Give the position of every malaria parasite.
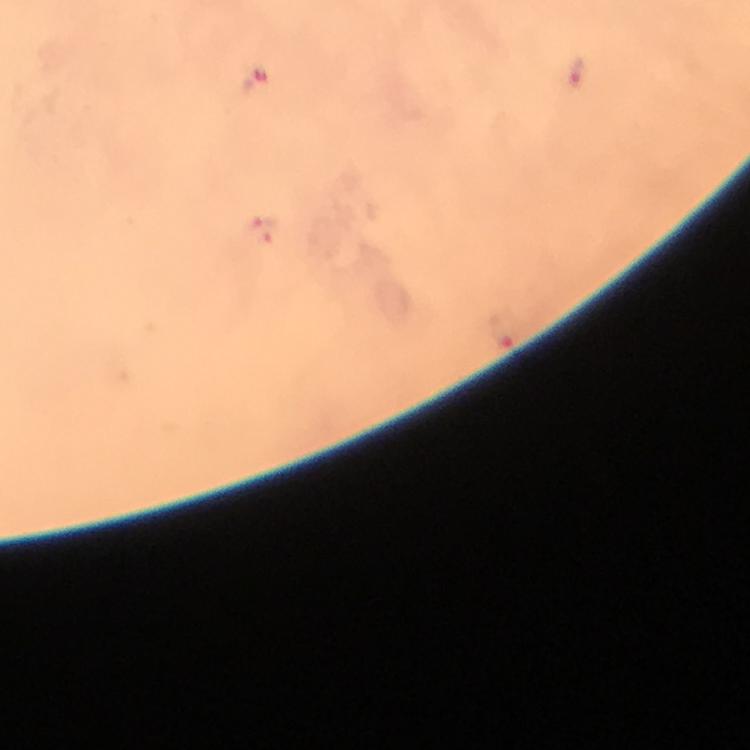
Approximate centers as {x, y} in pixels.
Malaria parasites: {576, 73}, {255, 80}, {260, 229}, {502, 331}.

context = from a diagnostic examination for malaria
preparation = thick smear
capture = smartphone photograph through a microscope
magnification = 100x
image size = 750×750 pixels
stain = Giemsa
cropped from = one field of view
immersion oil = applied